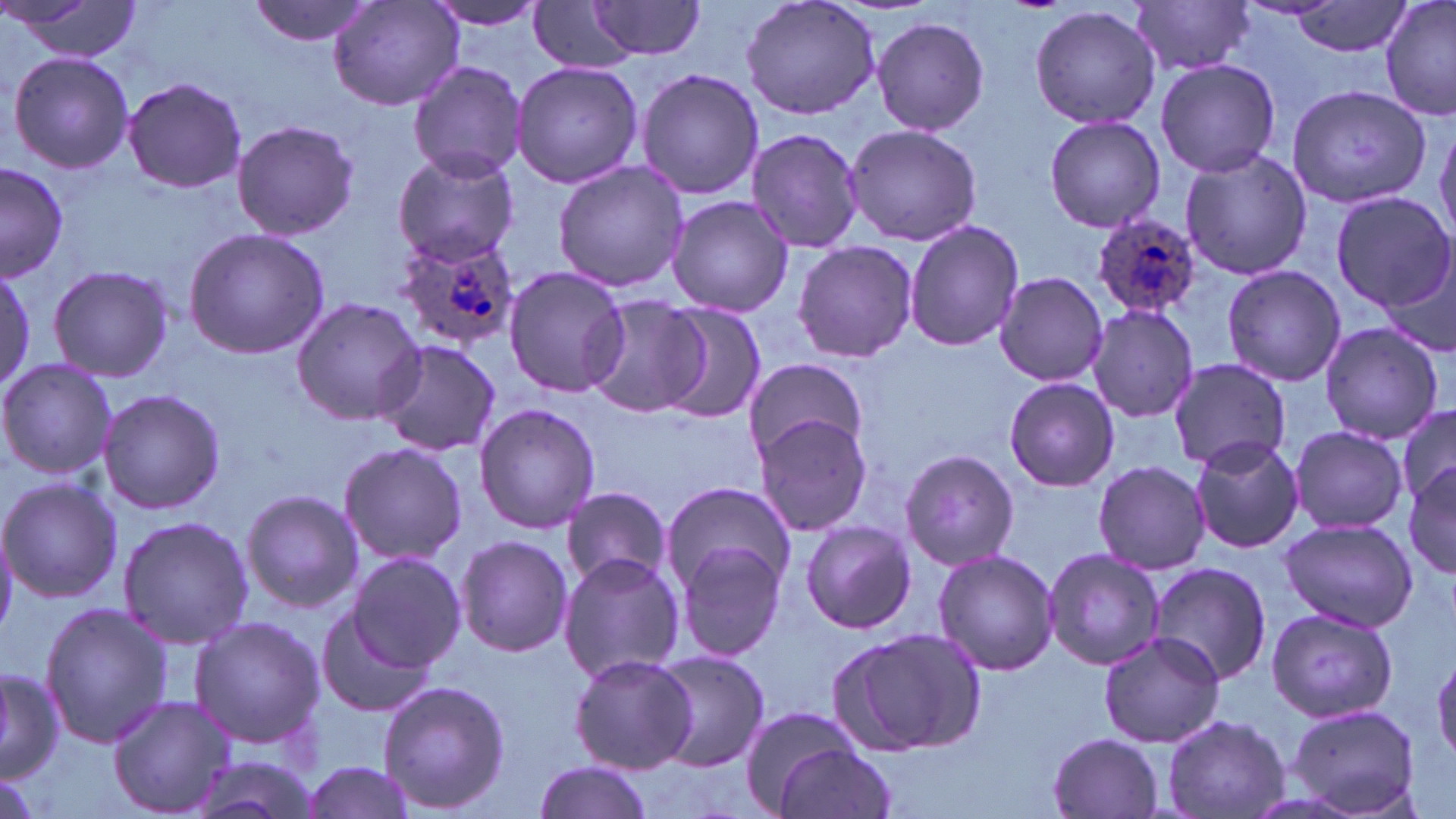 Approximate bounding boxes as [x1, y1, x2, y2] in pixels. Plasmodium ovale-infected red blood cell locations: [1093, 212, 1204, 321], [391, 233, 521, 350]. Uninfected red blood cell locations: [248, 0, 378, 46], [329, 0, 463, 113], [739, 0, 882, 120], [1380, 0, 1456, 122], [5, 1, 144, 63], [423, 1, 551, 31], [583, 1, 710, 61], [1131, 1, 1256, 77], [1289, 1, 1413, 58], [528, 3, 637, 74], [1029, 5, 1162, 131], [870, 14, 990, 135], [5, 52, 134, 173], [1156, 59, 1281, 178], [408, 61, 527, 181], [509, 61, 643, 190], [635, 68, 765, 200], [122, 76, 247, 194], [1282, 86, 1429, 204], [1042, 116, 1166, 234], [1435, 118, 1456, 246], [230, 119, 359, 242], [842, 123, 983, 245], [745, 126, 866, 254], [392, 148, 519, 267], [1178, 148, 1313, 281], [0, 161, 69, 280], [553, 161, 690, 293], [1329, 191, 1455, 311], [665, 195, 794, 317], [905, 218, 1024, 353], [183, 228, 332, 360], [792, 240, 918, 361], [1379, 254, 1455, 362], [0, 260, 35, 393], [48, 264, 174, 383], [1222, 265, 1347, 387], [503, 267, 629, 399], [991, 271, 1107, 386], [581, 296, 708, 418], [290, 297, 424, 425], [654, 304, 766, 421], [1086, 305, 1200, 424], [1318, 322, 1445, 444], [371, 340, 502, 458], [0, 358, 116, 482], [1168, 358, 1291, 470], [742, 359, 868, 458], [1003, 377, 1119, 492], [97, 387, 226, 516], [474, 402, 600, 534], [1393, 403, 1456, 513], [750, 411, 875, 536], [1287, 425, 1408, 534], [1189, 434, 1305, 555], [338, 441, 470, 568], [899, 448, 1020, 572], [1093, 461, 1208, 573], [1404, 464, 1456, 579], [0, 476, 121, 604], [661, 480, 797, 595], [561, 487, 672, 592], [239, 489, 363, 613], [118, 516, 255, 649], [1279, 517, 1419, 633], [799, 520, 916, 635], [455, 535, 574, 659], [674, 541, 788, 663], [1042, 547, 1167, 671], [932, 550, 1061, 677], [347, 551, 467, 673], [559, 555, 686, 683], [1146, 562, 1273, 687], [39, 600, 171, 748], [315, 604, 440, 720], [1266, 608, 1397, 722], [189, 615, 327, 749], [828, 624, 987, 757], [1097, 632, 1225, 748], [650, 650, 770, 770], [568, 653, 696, 773], [0, 665, 63, 783], [375, 679, 511, 815], [108, 695, 233, 816], [1284, 702, 1423, 818], [735, 704, 866, 813], [1162, 714, 1288, 818], [1045, 732, 1166, 818], [770, 740, 898, 819], [183, 754, 324, 819], [298, 758, 422, 819], [533, 758, 656, 819]. Slide-level diagnosis: Plasmodium ovale. Thin blood smear. Image is 1456×819 pixels. Light microscopy. One field of a larger specimen. 1000x magnification. May-Grünwald-Giemsa-stained preparation.